Locate and identify every blood parasite.
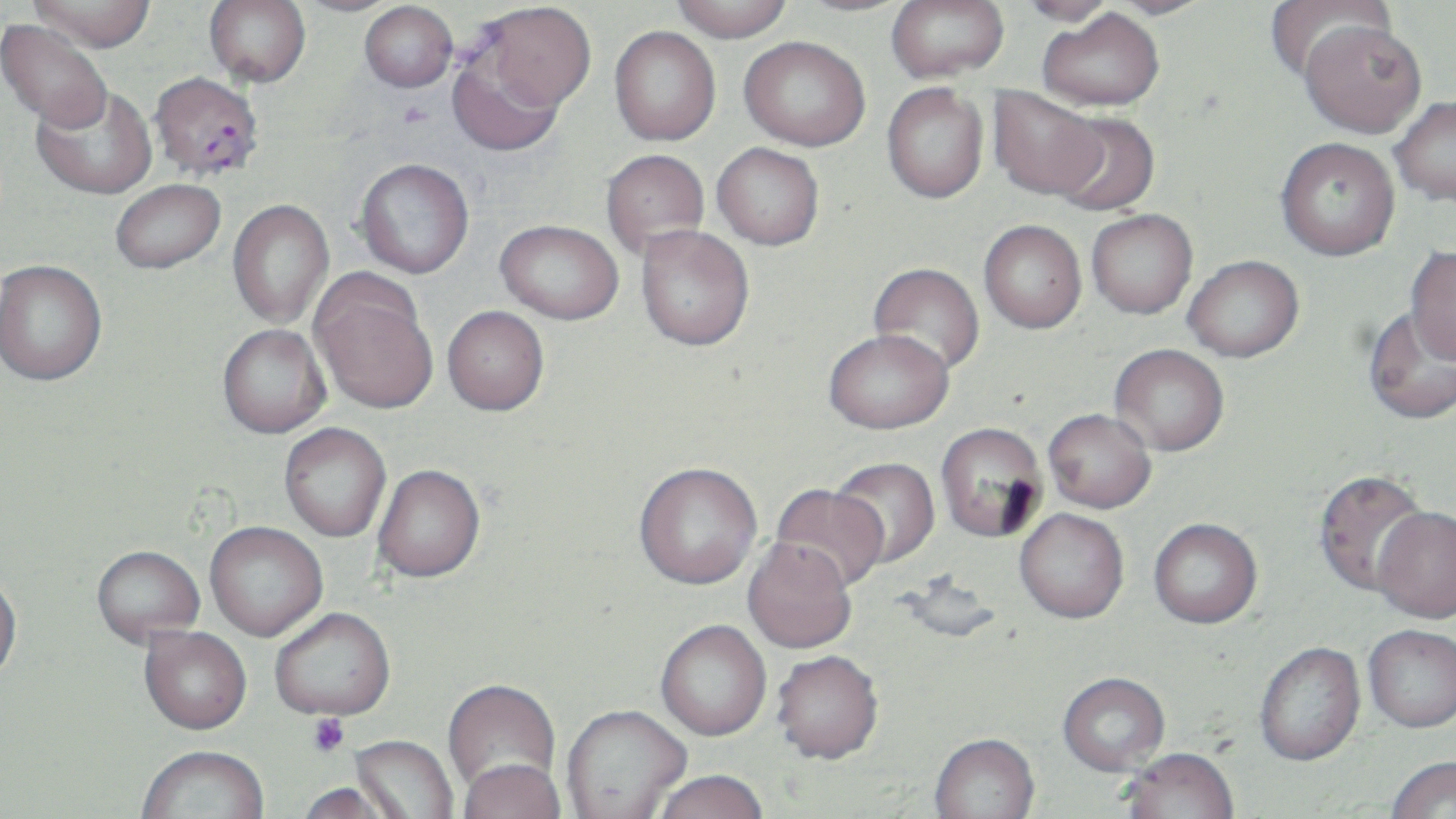
Approximate bounding boxes as named x1/y1/x2/y2 corners in pixels.
Plasmodium falciparum-infected red blood cells: (x1=149, y1=72, x2=264, y2=181).
No Plasmodium ovale, Plasmodium malariae, Plasmodium vivax, Babesia divergens, or Trypanosoma brucei observed.

slide-level diagnosis = Plasmodium falciparum
image size = 1456×819 pixels
platelet locations = approximate bounding boxes as named x1/y1/x2/y2 corners in pixels: (x1=308, y1=714, x2=351, y2=757)
preparation = thin blood smear
field of view = one of a larger specimen
modality = light microscopy
stain = May-Grünwald-Giemsa
magnification = 1000x
uninfected red blood cell locations = approximate bounding boxes as named x1/y1/x2/y2 corners in pixels: (x1=29, y1=0, x2=156, y2=51), (x1=204, y1=0, x2=311, y2=87), (x1=290, y1=0, x2=406, y2=17), (x1=670, y1=0, x2=794, y2=41), (x1=788, y1=0, x2=918, y2=16), (x1=886, y1=0, x2=1009, y2=82), (x1=1016, y1=0, x2=1118, y2=26), (x1=1101, y1=0, x2=1217, y2=19), (x1=1264, y1=0, x2=1395, y2=83), (x1=359, y1=1, x2=458, y2=92), (x1=477, y1=2, x2=596, y2=114), (x1=1038, y1=8, x2=1164, y2=111), (x1=1, y1=18, x2=113, y2=132), (x1=1299, y1=20, x2=1427, y2=138), (x1=609, y1=26, x2=721, y2=145), (x1=739, y1=36, x2=870, y2=151), (x1=447, y1=48, x2=566, y2=158), (x1=881, y1=83, x2=988, y2=203), (x1=32, y1=85, x2=157, y2=200), (x1=987, y1=86, x2=1105, y2=201), (x1=1390, y1=95, x2=1456, y2=206), (x1=1050, y1=110, x2=1161, y2=216), (x1=1276, y1=137, x2=1400, y2=260), (x1=712, y1=143, x2=824, y2=250), (x1=600, y1=149, x2=710, y2=260), (x1=355, y1=158, x2=474, y2=278), (x1=110, y1=179, x2=225, y2=274), (x1=227, y1=199, x2=334, y2=329), (x1=1086, y1=209, x2=1198, y2=319), (x1=495, y1=219, x2=623, y2=324), (x1=979, y1=220, x2=1087, y2=333), (x1=636, y1=225, x2=755, y2=352), (x1=1405, y1=245, x2=1456, y2=363), (x1=1183, y1=255, x2=1304, y2=362), (x1=0, y1=259, x2=107, y2=386), (x1=868, y1=262, x2=985, y2=376), (x1=310, y1=273, x2=439, y2=416), (x1=442, y1=306, x2=549, y2=417), (x1=1361, y1=306, x2=1456, y2=427), (x1=217, y1=324, x2=331, y2=440), (x1=823, y1=329, x2=954, y2=435), (x1=1110, y1=344, x2=1229, y2=456), (x1=1042, y1=409, x2=1156, y2=514), (x1=935, y1=423, x2=1048, y2=544), (x1=279, y1=424, x2=391, y2=543), (x1=830, y1=459, x2=940, y2=570), (x1=634, y1=464, x2=763, y2=593), (x1=373, y1=467, x2=486, y2=586), (x1=1313, y1=469, x2=1433, y2=598), (x1=770, y1=484, x2=888, y2=594), (x1=1372, y1=507, x2=1456, y2=625), (x1=1015, y1=510, x2=1129, y2=626), (x1=1148, y1=520, x2=1262, y2=632), (x1=205, y1=524, x2=328, y2=642), (x1=742, y1=542, x2=856, y2=655), (x1=92, y1=548, x2=205, y2=649), (x1=897, y1=568, x2=1005, y2=646), (x1=0, y1=574, x2=22, y2=688), (x1=270, y1=610, x2=396, y2=725), (x1=656, y1=622, x2=771, y2=743), (x1=1364, y1=627, x2=1456, y2=735), (x1=139, y1=628, x2=252, y2=737), (x1=1255, y1=644, x2=1366, y2=768), (x1=770, y1=653, x2=884, y2=769), (x1=1058, y1=675, x2=1170, y2=778), (x1=442, y1=680, x2=561, y2=803), (x1=562, y1=707, x2=690, y2=819), (x1=349, y1=736, x2=458, y2=819), (x1=929, y1=736, x2=1040, y2=819), (x1=137, y1=748, x2=270, y2=819), (x1=1119, y1=751, x2=1239, y2=819), (x1=1386, y1=758, x2=1456, y2=819), (x1=459, y1=762, x2=566, y2=819), (x1=652, y1=773, x2=769, y2=819), (x1=295, y1=784, x2=402, y2=819)